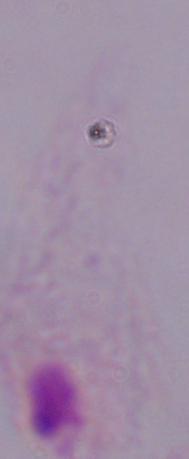
magnification = 1000x
modality = micrograph
identification = trichomonad